Comment on the morphology of the erythrocytes.
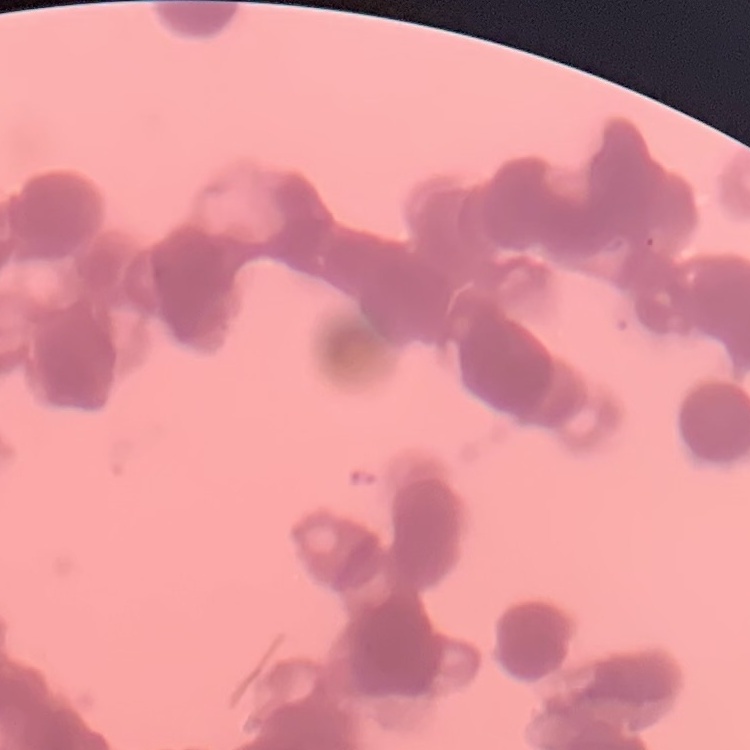
They show rouleaux formation.

preparation = thin peripheral smear
stain = Field's or Giemsa
image type = one tile cut from a larger photomicrograph